Describe the morphology of the erythrocytes.
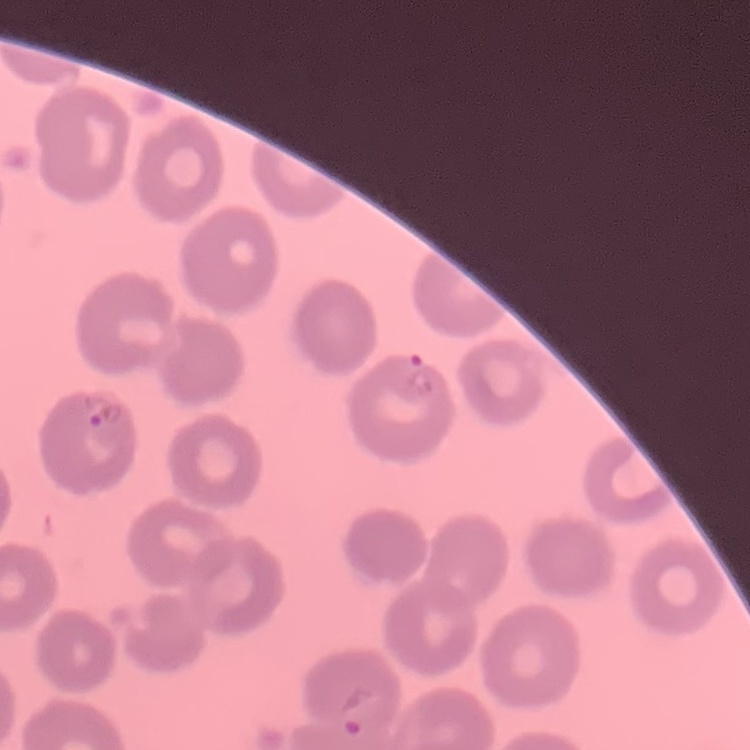
No rouleaux formation.

Summary:
  - Preparation: thin peripheral smear
  - Image type: one tile cut from a larger photomicrograph
  - Stain: Field's or Giemsa